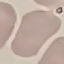

Summary:
  - Malaria status: uninfected
  - Stain: Giemsa
  - Capture: smartphone camera at the microscope eyepiece
  - Image type: automatically extracted cell patch, resized to 64 × 64 pixels
  - Preparation: thin blood smear